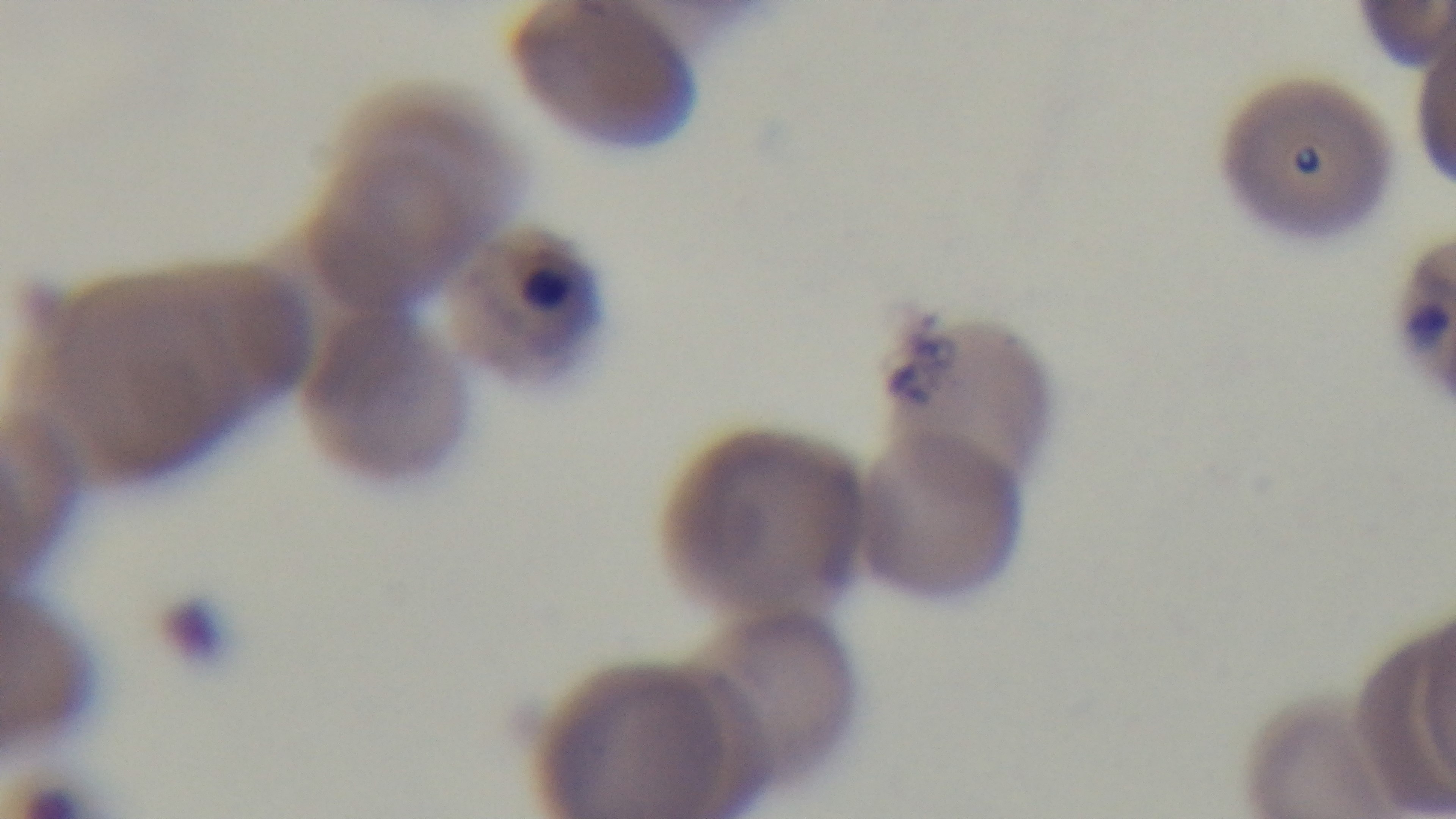

stain: Giemsa
capture: mounted 4K digital camera
preparation: thin blood film
malaria_status: positive
objective: 100x oil immersion
modality: light microscopy
field_of_view: one from the slide